Describe the morphology of the red blood cells.
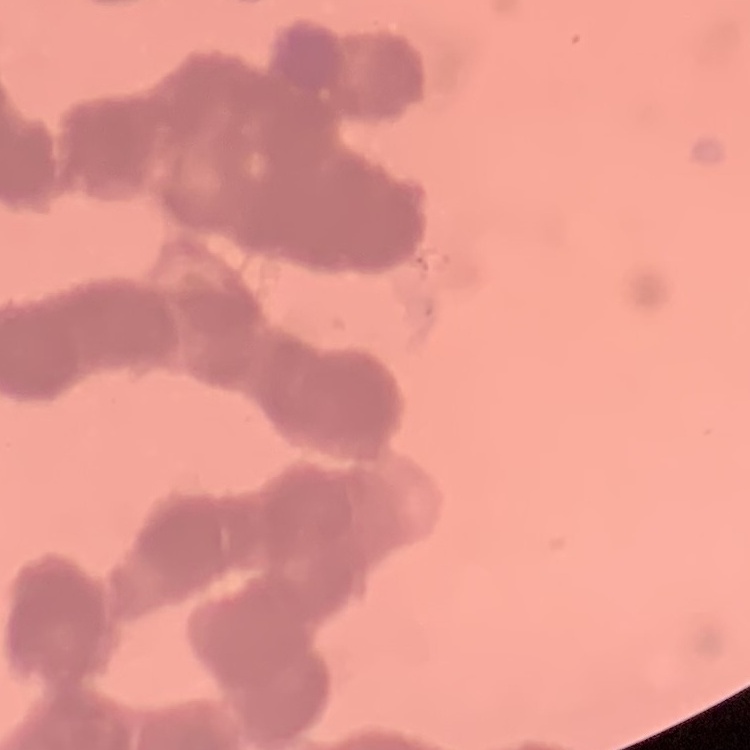

Rouleaux formation.

stain = Field's or Giemsa
image type = square crop of a larger photomicrograph
preparation = thin blood smear